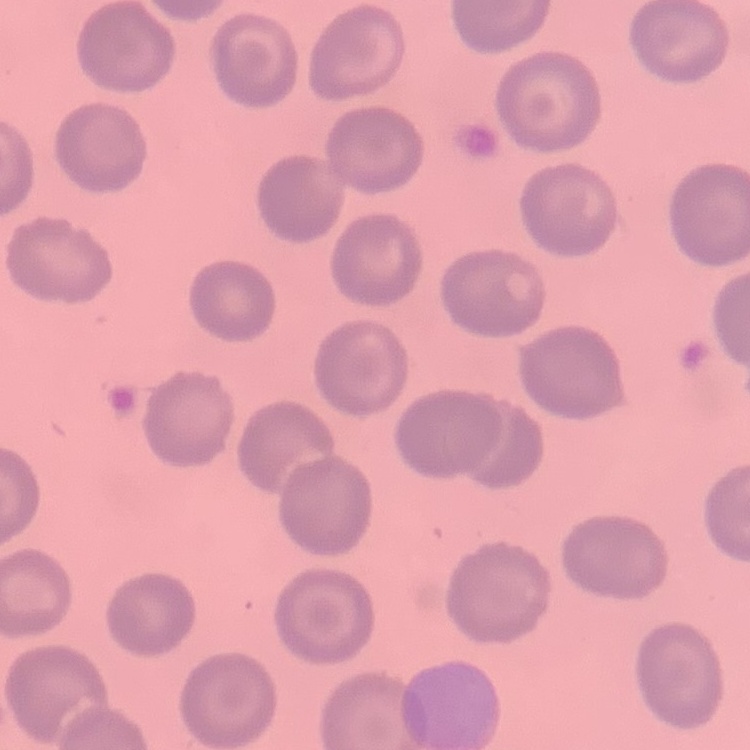
{
  "erythrocyte_morphology": "no rouleaux formation",
  "preparation": "thin blood film",
  "stain": "Field's or Giemsa",
  "image_type": "one tile cut from a larger photomicrograph"
}